Locate every Plasmodium ovale-infected red blood cell.
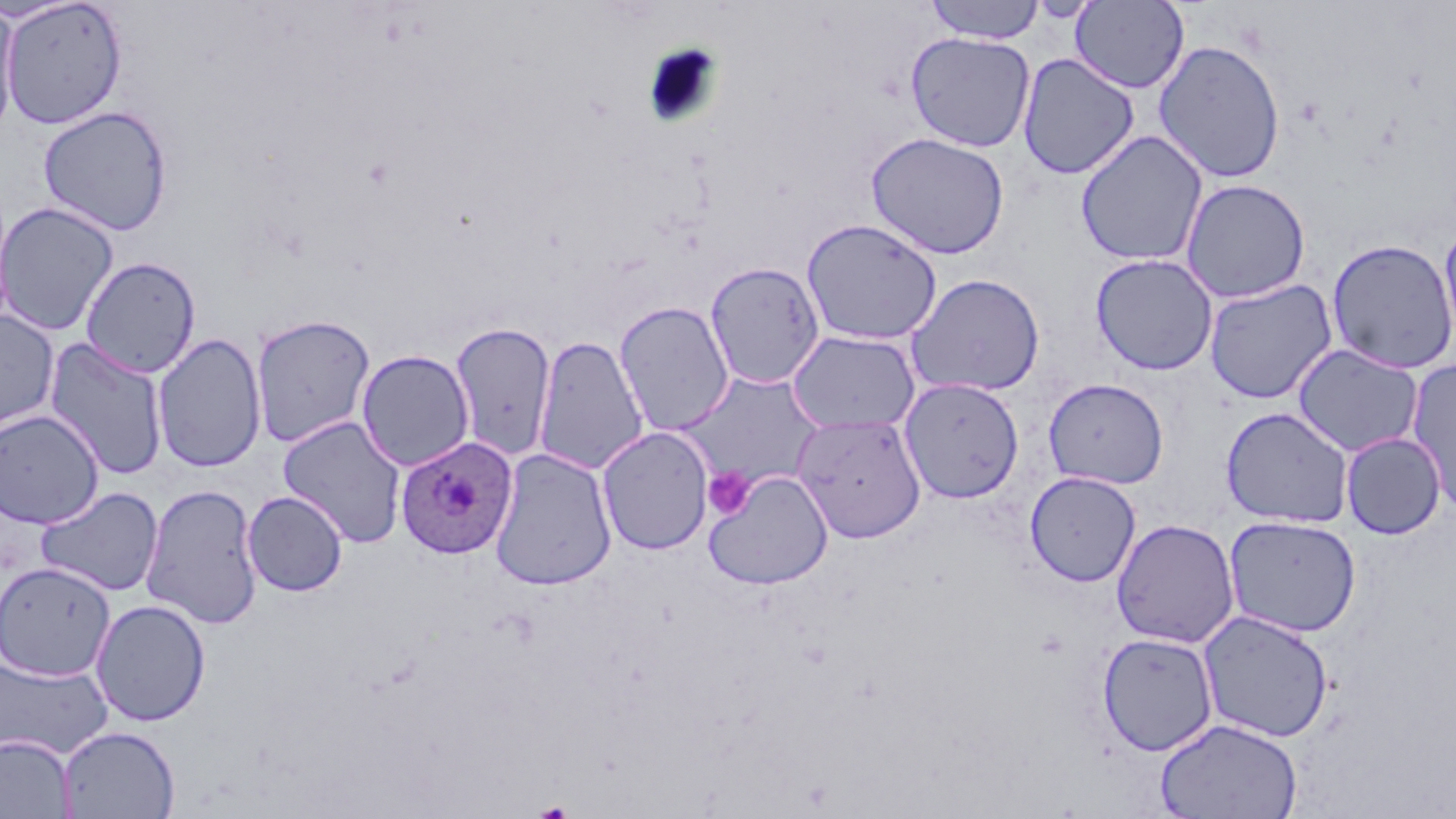
Approximate bounding boxes as named x1/y1/x2/y2 corners in pixels.
Plasmodium ovale-infected red blood cells: (x1=395, y1=436, x2=517, y2=559).

Uninfected red blood cell locations: (x1=923, y1=0, x2=1047, y2=44), (x1=1, y1=1, x2=128, y2=129), (x1=1069, y1=1, x2=1190, y2=94), (x1=0, y1=2, x2=20, y2=139), (x1=905, y1=31, x2=1036, y2=153), (x1=1152, y1=39, x2=1287, y2=184), (x1=1017, y1=53, x2=1140, y2=180), (x1=38, y1=106, x2=173, y2=236), (x1=1075, y1=130, x2=1209, y2=267), (x1=865, y1=132, x2=1010, y2=260), (x1=1180, y1=178, x2=1311, y2=304), (x1=0, y1=201, x2=119, y2=336), (x1=800, y1=218, x2=942, y2=345), (x1=1437, y1=219, x2=1456, y2=357), (x1=1325, y1=238, x2=1456, y2=374), (x1=1090, y1=253, x2=1219, y2=375), (x1=81, y1=256, x2=201, y2=378), (x1=705, y1=261, x2=825, y2=389), (x1=906, y1=273, x2=1045, y2=397), (x1=1203, y1=278, x2=1338, y2=404), (x1=613, y1=300, x2=736, y2=437), (x1=0, y1=309, x2=60, y2=433), (x1=251, y1=313, x2=376, y2=447), (x1=449, y1=321, x2=557, y2=461), (x1=786, y1=329, x2=921, y2=434), (x1=152, y1=333, x2=267, y2=472), (x1=533, y1=334, x2=650, y2=476), (x1=43, y1=337, x2=169, y2=480), (x1=1292, y1=343, x2=1424, y2=457), (x1=356, y1=349, x2=475, y2=471), (x1=1406, y1=358, x2=1456, y2=515), (x1=679, y1=371, x2=826, y2=491), (x1=900, y1=377, x2=1025, y2=504), (x1=1042, y1=377, x2=1168, y2=489), (x1=1221, y1=406, x2=1354, y2=528), (x1=0, y1=409, x2=105, y2=529), (x1=792, y1=412, x2=927, y2=543), (x1=277, y1=415, x2=407, y2=548), (x1=596, y1=426, x2=714, y2=556), (x1=1340, y1=432, x2=1446, y2=540), (x1=489, y1=448, x2=617, y2=590), (x1=704, y1=471, x2=834, y2=591), (x1=1024, y1=471, x2=1141, y2=587), (x1=141, y1=482, x2=263, y2=629), (x1=35, y1=486, x2=164, y2=597), (x1=242, y1=490, x2=348, y2=597), (x1=1223, y1=515, x2=1361, y2=637), (x1=1111, y1=518, x2=1240, y2=649), (x1=0, y1=561, x2=115, y2=681), (x1=90, y1=599, x2=211, y2=726), (x1=1198, y1=609, x2=1334, y2=743), (x1=1096, y1=632, x2=1219, y2=756), (x1=0, y1=654, x2=113, y2=760), (x1=1154, y1=717, x2=1303, y2=819), (x1=58, y1=726, x2=180, y2=818), (x1=0, y1=734, x2=75, y2=819). Platelet locations: (x1=703, y1=467, x2=754, y2=520). Slide-level diagnosis: Plasmodium ovale. One field of a larger specimen. Thin blood smear. Captured at 1000x magnification. Image is 1456×819 pixels. May-Grünwald-Giemsa stain. Optical microscopy.